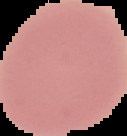

image size = 127×136 pixels
image type = segmented cell region with the area outside set to black
preparation = thin blood smear
malaria status = uninfected